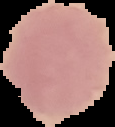
preparation: thin blood film
result: no Plasmodium parasites detected
image_type: segmented cell region on a black background
image_size: 115×127 pixels